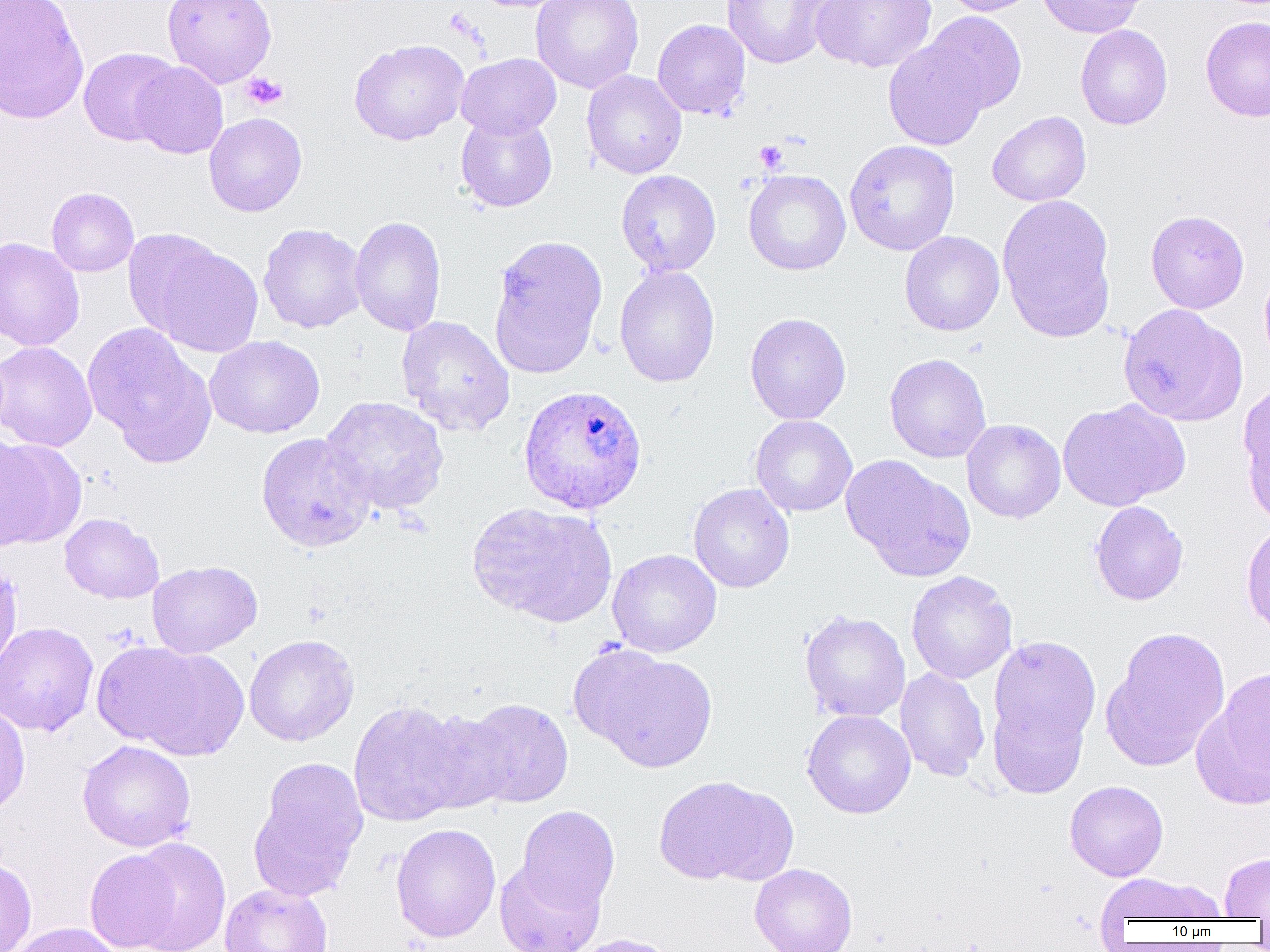

Approximate bounding boxes as [x1, y1, x2, y2] in pixels. Uninfected red blood cell locations: [0, 0, 89, 124], [163, 0, 277, 88], [531, 0, 644, 93], [811, 0, 936, 72], [940, 0, 1041, 16], [1036, 0, 1148, 38], [720, 1, 844, 69], [920, 12, 1027, 115], [1200, 15, 1270, 122], [652, 19, 751, 120], [1075, 24, 1173, 130], [883, 35, 993, 152], [349, 38, 469, 145], [78, 47, 182, 146], [456, 52, 561, 139], [131, 61, 228, 159], [581, 70, 687, 179], [987, 111, 1091, 207], [204, 112, 307, 217], [456, 113, 557, 212], [844, 139, 960, 256], [743, 169, 851, 275], [616, 170, 721, 277], [46, 187, 139, 277], [997, 194, 1117, 343], [1146, 209, 1249, 314], [349, 215, 447, 337], [258, 223, 367, 334], [899, 231, 1005, 336], [487, 234, 609, 379], [0, 237, 85, 351], [137, 237, 264, 358], [1259, 264, 1270, 370], [614, 266, 720, 387], [1117, 303, 1248, 427], [744, 313, 851, 424], [396, 315, 516, 437], [83, 323, 216, 465], [205, 335, 325, 439], [0, 341, 97, 452], [884, 353, 992, 463], [1238, 381, 1270, 526], [320, 395, 449, 516], [1057, 399, 1190, 511], [750, 415, 857, 517], [961, 419, 1066, 523], [256, 432, 376, 552], [0, 437, 82, 550], [840, 455, 976, 582], [688, 483, 795, 593], [467, 501, 617, 627], [1090, 501, 1188, 606], [59, 513, 164, 604], [1240, 520, 1270, 638], [607, 549, 722, 657], [147, 560, 262, 658], [0, 561, 22, 675], [906, 571, 1017, 684], [800, 610, 911, 723], [0, 621, 99, 737], [1102, 626, 1231, 771], [244, 634, 359, 746], [988, 635, 1102, 758], [92, 641, 207, 748], [129, 646, 249, 760], [576, 646, 718, 772], [895, 667, 990, 782], [1193, 670, 1270, 809], [988, 695, 1091, 798], [460, 698, 574, 808], [0, 700, 30, 818], [348, 700, 470, 826], [802, 709, 916, 818], [413, 710, 517, 815], [77, 740, 196, 852], [250, 757, 368, 900], [653, 775, 795, 886], [1064, 780, 1169, 881], [516, 805, 620, 915], [391, 823, 501, 942], [128, 837, 231, 952], [85, 849, 181, 952], [1220, 853, 1270, 919], [0, 858, 37, 952], [494, 858, 604, 952], [749, 863, 858, 952], [1095, 873, 1224, 923], [219, 883, 333, 952], [10, 922, 122, 952], [566, 933, 681, 952]. Plasmodium ovale-infected red blood cell locations: [518, 383, 648, 514]. Platelet locations: [241, 72, 288, 110], [754, 140, 787, 173]. Slide-level diagnosis: Plasmodium ovale. Image is 1270×952 pixels. Single field of view. Captured at 1000x magnification. Thin blood smear. Light microscopy.